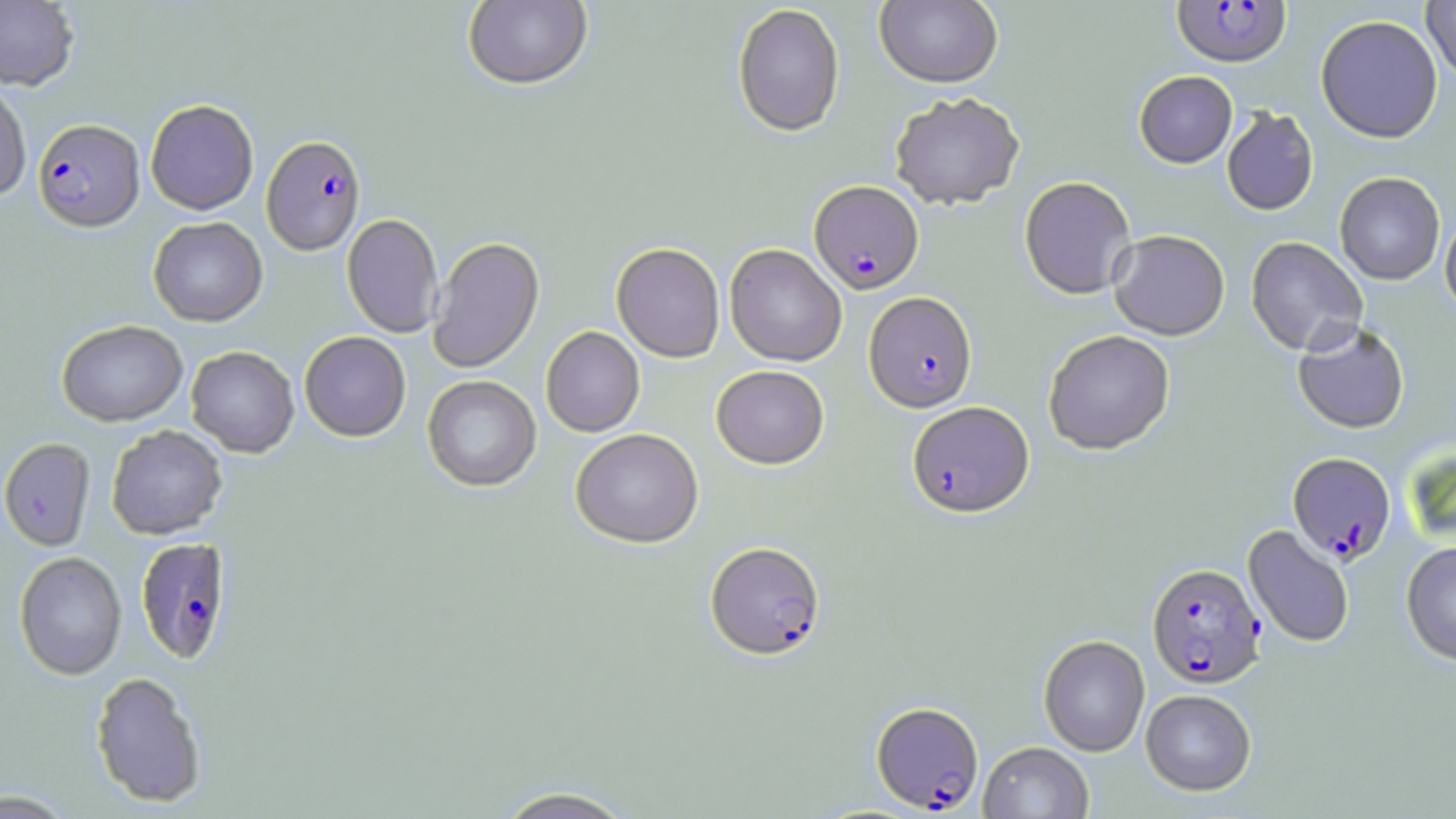

slide_level_diagnosis: Plasmodium falciparum
preparation: thin blood film
field_of_view: one of a larger specimen
uninfected_red_blood_cell_locations: 'approximate bounding boxes as (x1,y1)-(x2,y2) corner pairs in pixels: (0,0)-(79,91), (462,0)-(594,91), (874,0)-(1003,89), (1422,0)-(1456,82), (732,4)-(845,138), (1315,15)-(1443,145), (1134,71)-(1237,169), (0,80)-(32,203), (890,94)-(1025,211), (145,99)-(259,215), (1222,108)-(1319,217), (1334,173)-(1445,286), (1020,178)-(1137,301), (1440,210)-(1456,319), (342,214)-(443,337), (148,216)-(267,327), (1109,231)-(1230,341), (428,237)-(545,373), (1246,237)-(1367,357), (611,243)-(725,363), (725,244)-(847,367), (57,319)-(188,426), (1292,322)-(1410,435), (541,326)-(645,437), (1043,331)-(1175,456), (299,332)-(411,442), (186,346)-(299,457), (711,365)-(829,469), (422,375)-(542,493), (106,425)-(228,540), (570,428)-(704,549), (0,438)-(95,551), (1243,525)-(1354,649), (1401,541)-(1456,667), (14,552)-(127,680), (1039,635)-(1150,757), (90,671)-(208,808), (1141,689)-(1256,796), (978,742)-(1093,818), (491,786)-(640,819), (0,789)-(77,816)'
modality: light microscopy
plasmodium_falciparum_infected_red_blood_cell_locations: 'approximate bounding boxes as (x1,y1)-(x2,y2) corner pairs in pixels: (1171,1)-(1291,69), (33,119)-(145,231), (261,135)-(366,255), (809,180)-(924,294), (864,293)-(977,413), (907,402)-(1034,519), (1287,453)-(1395,565), (134,537)-(233,665), (705,542)-(825,661), (1147,563)-(1266,689), (871,702)-(984,813)'
image_size: 1456×819 pixels
magnification: 1000x
stain: May-Grünwald-Giemsa